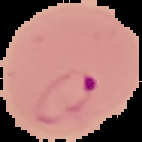
Segmented cell region on a black background. From a thin blood film. Image is 142×142 pixels. Malaria status: parasitized.